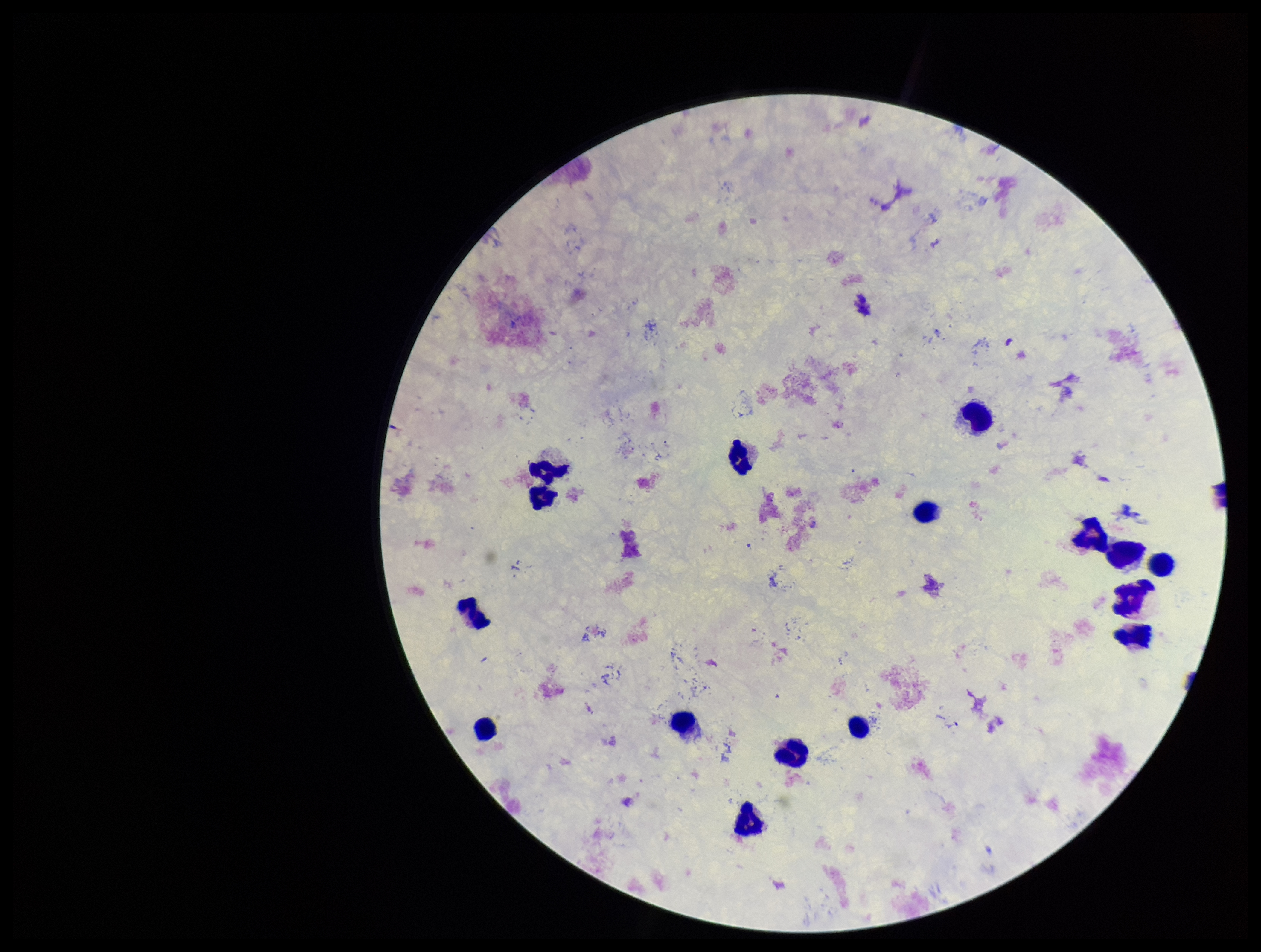

Smartphone photograph taken through the eyepiece of a microscope. Leukocyte count: 16. Image is 1261×952 pixels. Parasite count: 0. Stained with Giemsa. Preparation: thick blood smear. Single field of view. Patient malaria status: negative. Plasmodium parasites: none identified.